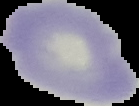
Summary:
  - Image size: 139×106 pixels
  - Image type: segmented cell region on a black background
  - Result: no Plasmodium parasites seen
  - Preparation: thin blood smear